Give the preparation type.
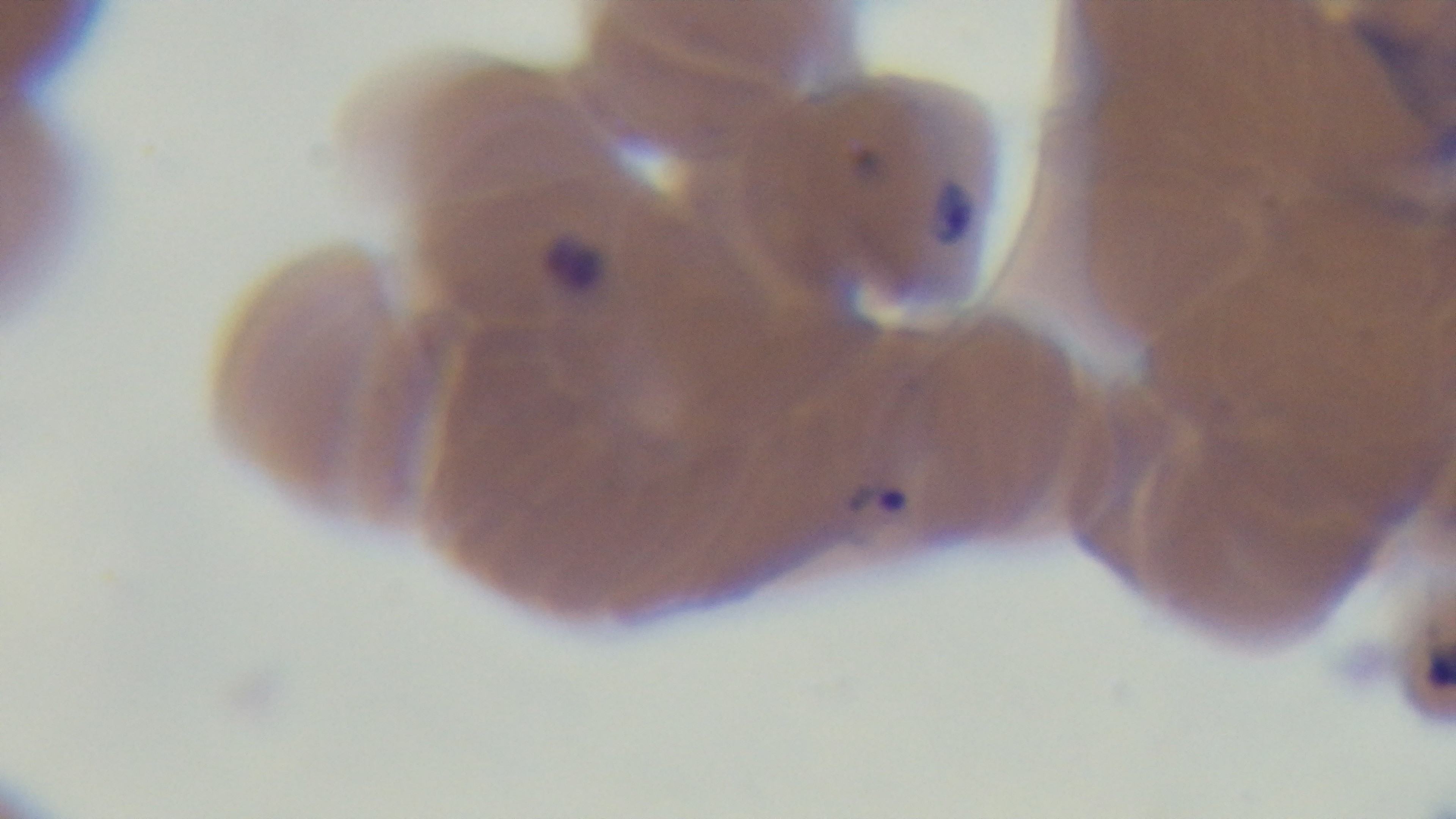
A thin smear.

Summary:
  - Field of view: single
  - Capture: mounted 4K digital camera
  - Objective: 100x oil immersion
  - Malaria status: infected
  - Stain: Giemsa
  - Modality: light microscopy